Assess this cell for malaria.
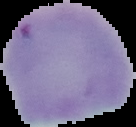

Parasitized.

image_size: 136×127 pixels
image_type: segmented cell region with the area outside set to black
preparation: thin blood film